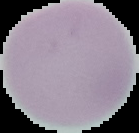
{
  "image_type": "segmented cell region on a black background",
  "preparation": "thin blood film",
  "result": "no Plasmodium parasites seen",
  "image_size": "139×133 pixels"
}